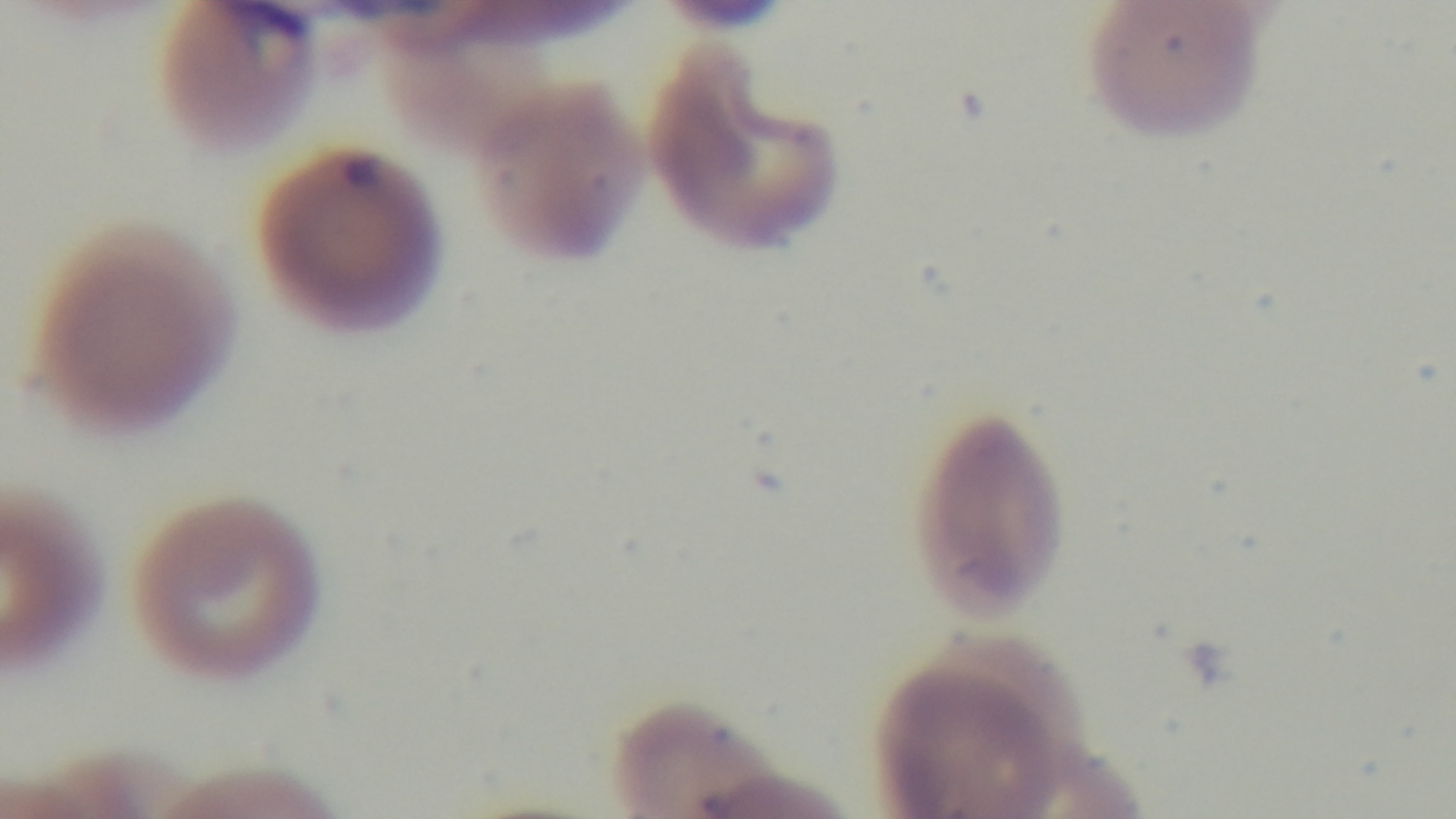
Summary:
  - Capture: mounted 4K digital camera
  - Modality: light microscopy
  - Stain: Giemsa
  - Objective: 100x oil immersion
  - Field of view: single
  - Preparation: thin
  - Malaria status: positive